Outline every Plasmodium parasite.
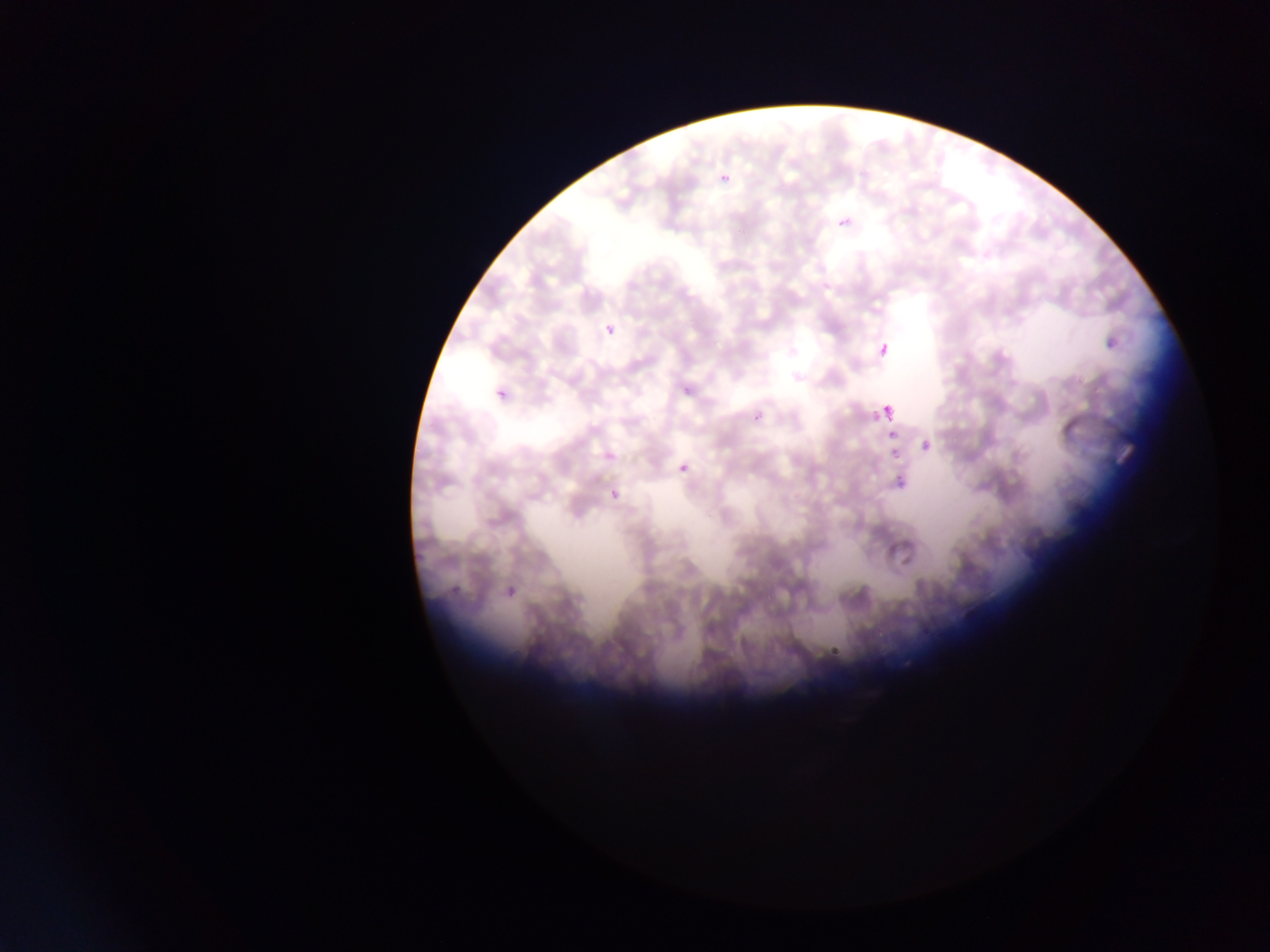

Approximate bounding boxes as (left, top, right, bottom) in pixels.
Plasmodium parasites: (720, 173, 729, 184), (835, 222, 854, 232), (605, 322, 616, 336), (876, 332, 895, 363), (682, 384, 692, 395), (494, 390, 506, 403), (883, 402, 907, 415), (750, 404, 765, 425), (865, 410, 883, 423), (887, 429, 898, 439), (919, 437, 932, 452), (886, 452, 900, 464), (678, 463, 689, 474), (891, 475, 908, 496), (599, 494, 618, 508), (504, 568, 525, 602), (446, 570, 475, 596), (825, 632, 849, 658).

capture = mobile-phone photograph through a microscope
preparation = thin blood smear
country = Ghana
image size = 1270×952 pixels
field of view = single